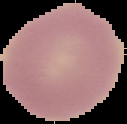
Cell region segmented out of the field of view; the surrounding area is masked to black. From a thin blood film. Image is 127×124 pixels. Result: negative for malaria parasites.